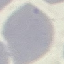

Malaria status: uninfected. Photographed with a smartphone camera at the microscope eyepiece. Automatically extracted cell patch, resized to 64 × 64 pixels. Giemsa-stained preparation. Thin blood smear.